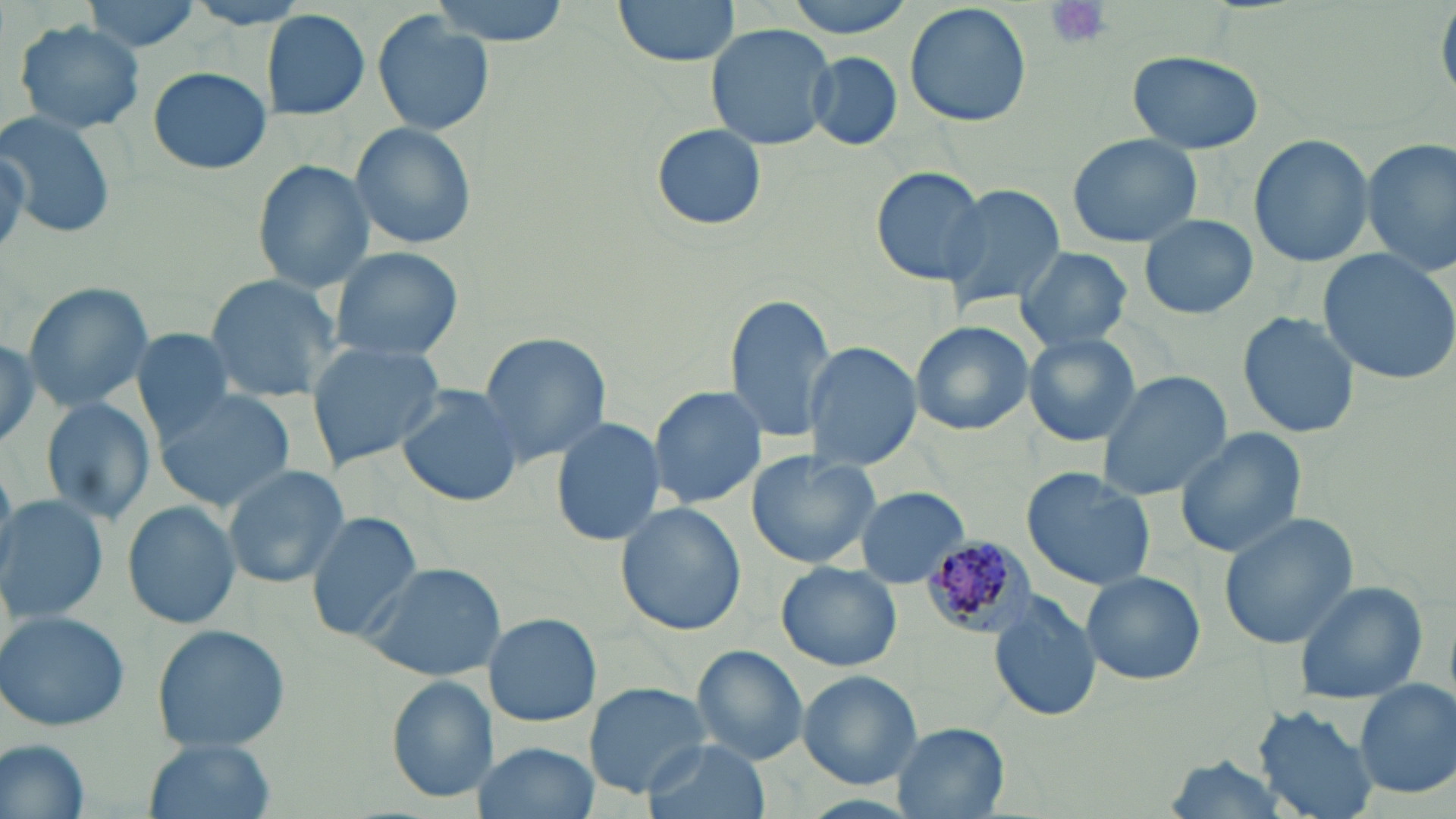
{
  "slide_level_diagnosis": "Plasmodium malariae",
  "stain": "May-Grünwald-Giemsa",
  "uninfected_red_blood_cell_locations": "approximate bounding boxes as (x1, y1, x2, y2) in pixels: (80, 0, 204, 55), (430, 0, 570, 44), (612, 0, 742, 67), (781, 0, 920, 37), (904, 2, 1033, 128), (261, 10, 371, 120), (371, 13, 491, 135), (13, 19, 147, 134), (704, 23, 837, 150), (1128, 50, 1264, 155), (805, 51, 903, 150), (148, 66, 271, 175), (0, 110, 117, 237), (348, 121, 478, 251), (650, 123, 768, 231), (1065, 133, 1202, 248), (1248, 133, 1375, 268), (1362, 138, 1455, 274), (253, 161, 375, 291), (870, 167, 989, 285), (936, 182, 1063, 313), (1137, 213, 1259, 320), (329, 246, 466, 365), (1317, 248, 1456, 385), (1015, 249, 1132, 353), (203, 274, 342, 397), (21, 280, 154, 413), (723, 292, 837, 443), (1239, 312, 1358, 438), (911, 321, 1033, 435), (131, 328, 238, 440), (0, 329, 47, 457), (477, 332, 611, 466), (1023, 333, 1142, 446), (304, 340, 445, 470), (802, 341, 921, 470), (1095, 370, 1233, 503), (396, 386, 523, 506), (648, 386, 767, 509), (156, 390, 299, 510), (40, 396, 155, 525), (550, 416, 665, 547), (1173, 426, 1308, 558), (745, 451, 880, 569), (221, 463, 351, 589), (1022, 467, 1157, 590), (853, 486, 967, 589), (0, 495, 109, 624), (121, 498, 241, 630), (618, 501, 745, 635), (304, 509, 426, 642), (1219, 512, 1358, 649), (356, 560, 505, 681), (777, 562, 903, 672), (1081, 571, 1205, 686), (1293, 579, 1428, 702), (990, 595, 1102, 722), (1, 610, 130, 732), (485, 611, 600, 727), (149, 623, 291, 753), (693, 645, 809, 764), (796, 671, 924, 788), (385, 676, 494, 803), (1354, 680, 1455, 799), (584, 681, 711, 796), (1255, 704, 1382, 819), (892, 724, 1010, 818), (141, 736, 277, 819), (1, 737, 91, 818), (642, 738, 770, 819), (480, 742, 598, 819)",
  "plasmodium_malariae_infected_red_blood_cell_locations": "approximate bounding boxes as (x1, y1, x2, y2) in pixels: (920, 533, 1030, 639)",
  "image_size": "1456×819 pixels",
  "platelet_locations": "approximate bounding boxes as (x1, y1, x2, y2) in pixels: (1044, 0, 1112, 50)",
  "preparation": "thin blood smear",
  "magnification": "1000x",
  "modality": "light microscopy",
  "field_of_view": "single"
}